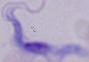

magnification: 1000x
identification: trypanosome
modality: micrograph